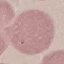
malaria_status: uninfected
preparation: thin blood smear
capture: smartphone through the microscope eyepiece
stain: Giemsa
image_type: cell patch, automatically extracted from a larger field of view and resized to 64 × 64 pixels